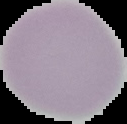

Summary:
  - Image size: 127×124 pixels
  - Image type: segmented cell region with the area outside set to black
  - Malaria status: uninfected
  - Preparation: thin blood smear